Identify the parasite.
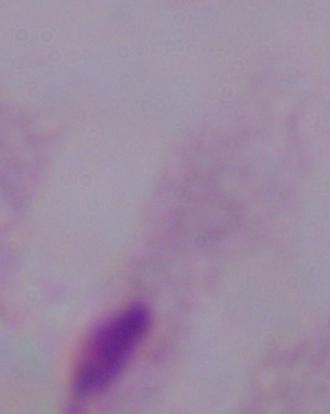

This is a trichomonad.

Summary:
  - Modality: photomicrograph
  - Magnification: 1000x